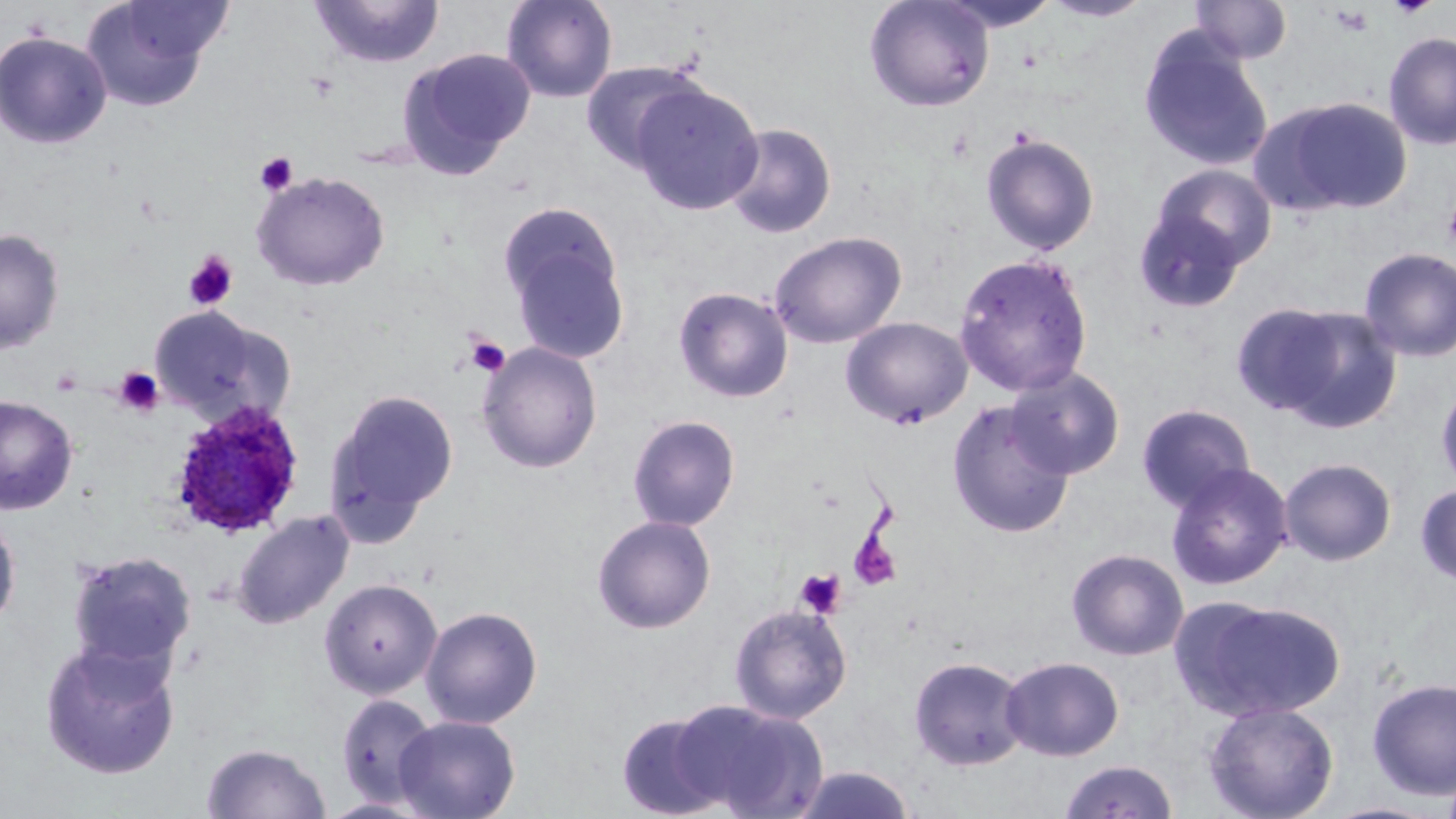

slide-level diagnosis = Plasmodium ovale
magnification = 1000x
Plasmodium ovale-infected red blood cell locations = approximate bounding boxes as named x1/y1/x2/y2 corners in pixels: (x1=169, y1=402, x2=305, y2=538)
modality = light microscopy
platelet locations = approximate bounding boxes as named x1/y1/x2/y2 corners in pixels: (x1=255, y1=152, x2=297, y2=196), (x1=1443, y1=201, x2=1456, y2=250), (x1=183, y1=251, x2=238, y2=311), (x1=465, y1=335, x2=510, y2=377), (x1=112, y1=366, x2=164, y2=417), (x1=848, y1=528, x2=902, y2=592), (x1=795, y1=568, x2=847, y2=619)
stain = May-Grünwald-Giemsa
field of view = single
uninfected red blood cell locations = approximate bounding boxes as named x1/y1/x2/y2 corners in pixels: (x1=310, y1=0, x2=445, y2=69), (x1=501, y1=0, x2=618, y2=103), (x1=864, y1=0, x2=994, y2=112), (x1=935, y1=0, x2=1062, y2=32), (x1=1190, y1=0, x2=1293, y2=64), (x1=114, y1=1, x2=235, y2=67), (x1=1041, y1=1, x2=1154, y2=23), (x1=80, y1=2, x2=221, y2=112), (x1=0, y1=30, x2=112, y2=149), (x1=1138, y1=30, x2=1273, y2=172), (x1=1383, y1=32, x2=1456, y2=150), (x1=397, y1=48, x2=536, y2=176), (x1=580, y1=60, x2=705, y2=173), (x1=631, y1=82, x2=764, y2=216), (x1=1256, y1=96, x2=1413, y2=217), (x1=723, y1=122, x2=836, y2=238), (x1=980, y1=132, x2=1100, y2=255), (x1=1152, y1=164, x2=1276, y2=270), (x1=252, y1=171, x2=390, y2=291), (x1=497, y1=201, x2=623, y2=315), (x1=1133, y1=207, x2=1248, y2=313), (x1=0, y1=228, x2=65, y2=355), (x1=768, y1=231, x2=907, y2=348), (x1=508, y1=236, x2=630, y2=363), (x1=1358, y1=247, x2=1456, y2=363), (x1=954, y1=252, x2=1093, y2=397), (x1=673, y1=287, x2=793, y2=403), (x1=1248, y1=303, x2=1401, y2=432), (x1=150, y1=305, x2=294, y2=425), (x1=841, y1=317, x2=973, y2=429), (x1=478, y1=342, x2=603, y2=473), (x1=1006, y1=366, x2=1125, y2=479), (x1=1435, y1=378, x2=1456, y2=494), (x1=325, y1=388, x2=458, y2=533), (x1=1, y1=395, x2=78, y2=515), (x1=948, y1=400, x2=1075, y2=538), (x1=1136, y1=404, x2=1256, y2=512), (x1=627, y1=414, x2=740, y2=531), (x1=1279, y1=457, x2=1397, y2=566), (x1=1165, y1=462, x2=1293, y2=591), (x1=1415, y1=484, x2=1456, y2=585), (x1=0, y1=508, x2=21, y2=635), (x1=231, y1=510, x2=354, y2=629), (x1=592, y1=515, x2=716, y2=634), (x1=1066, y1=548, x2=1189, y2=661), (x1=67, y1=550, x2=197, y2=672), (x1=319, y1=577, x2=442, y2=699), (x1=1182, y1=597, x2=1345, y2=721), (x1=729, y1=603, x2=852, y2=724), (x1=420, y1=606, x2=543, y2=729), (x1=39, y1=639, x2=181, y2=780), (x1=909, y1=656, x2=1028, y2=771), (x1=1000, y1=656, x2=1124, y2=761), (x1=1366, y1=677, x2=1456, y2=800), (x1=335, y1=694, x2=439, y2=807), (x1=671, y1=699, x2=827, y2=817), (x1=1203, y1=701, x2=1339, y2=819), (x1=616, y1=712, x2=731, y2=818), (x1=393, y1=715, x2=520, y2=819), (x1=201, y1=743, x2=331, y2=819), (x1=1059, y1=759, x2=1178, y2=819), (x1=1440, y1=764, x2=1456, y2=819), (x1=790, y1=765, x2=917, y2=819), (x1=1320, y1=801, x2=1444, y2=819)
image size = 1456×819 pixels
preparation = thin blood smear